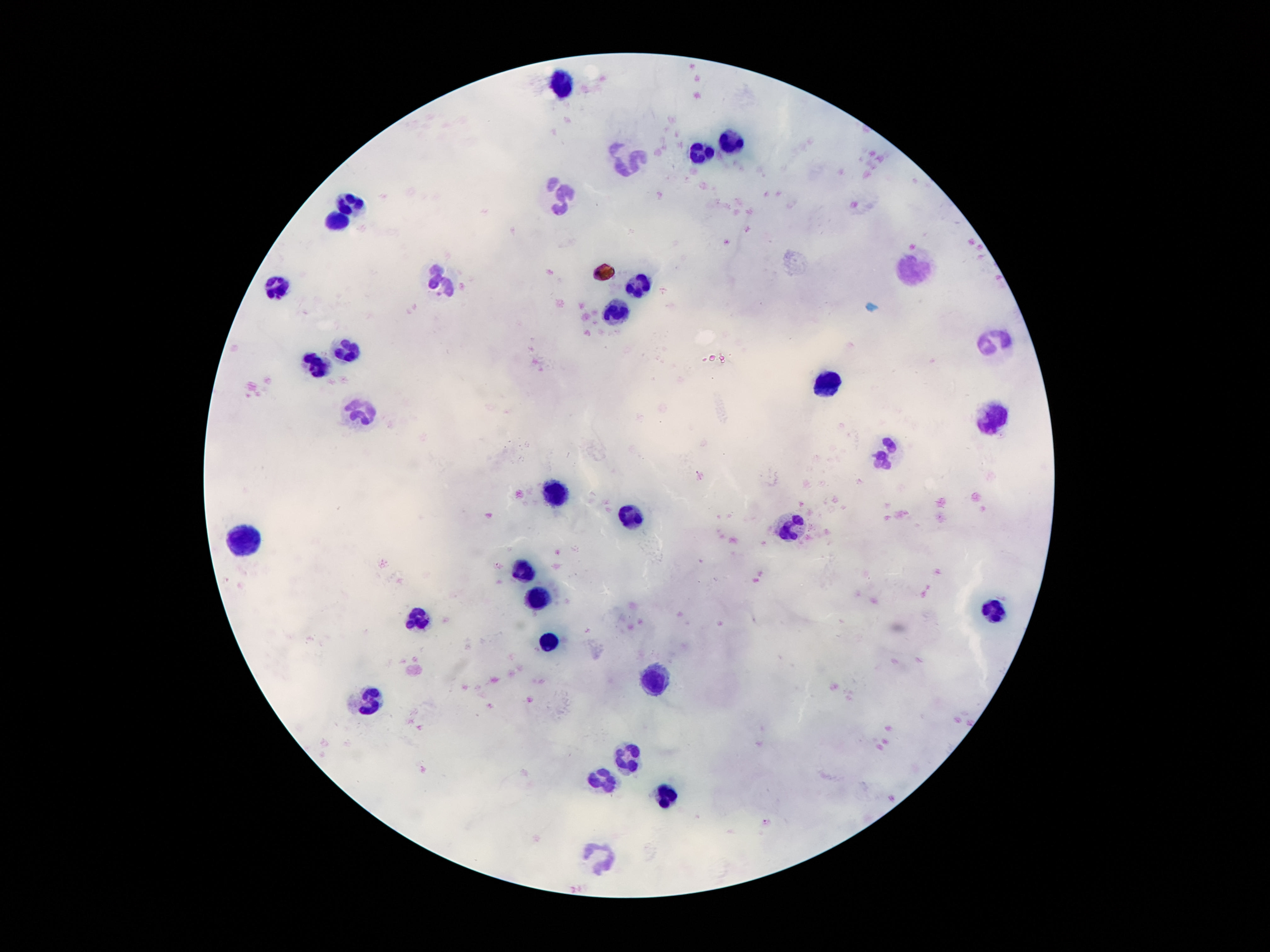
patient malaria status = negative
capture = smartphone camera through the microscope eyepiece
leukocyte locations = approximate centers as {x, y} in pixels: {561, 85}, {731, 138}, {701, 150}, {628, 162}, {559, 193}, {352, 200}, {339, 215}, {912, 269}, {441, 279}, {637, 285}, {283, 286}, {613, 312}, {997, 346}, {348, 351}, {316, 364}, {826, 381}, {361, 412}, {994, 416}, {885, 452}, {557, 491}, {630, 516}, {790, 531}, {245, 539}, {523, 567}, {538, 597}, {996, 612}, {419, 615}, {549, 640}, {658, 675}, {370, 701}, {628, 756}, {604, 779}, {661, 793}, {600, 858}
field of view = single
image size = 1270×952 pixels
magnification = 100x
stain = Giemsa
preparation = thick blood smear